Classify this cell by malaria status.
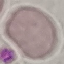
It is uninfected.

Summary:
  - Image type: automatically extracted cell patch, resized to 64 × 64 pixels
  - Capture: smartphone camera at the microscope eyepiece
  - Stain: Giemsa
  - Preparation: thin smear